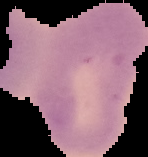

preparation: thin blood film
image_type: segmented cell region on a black background
image_size: 148×157 pixels
malaria_status: uninfected